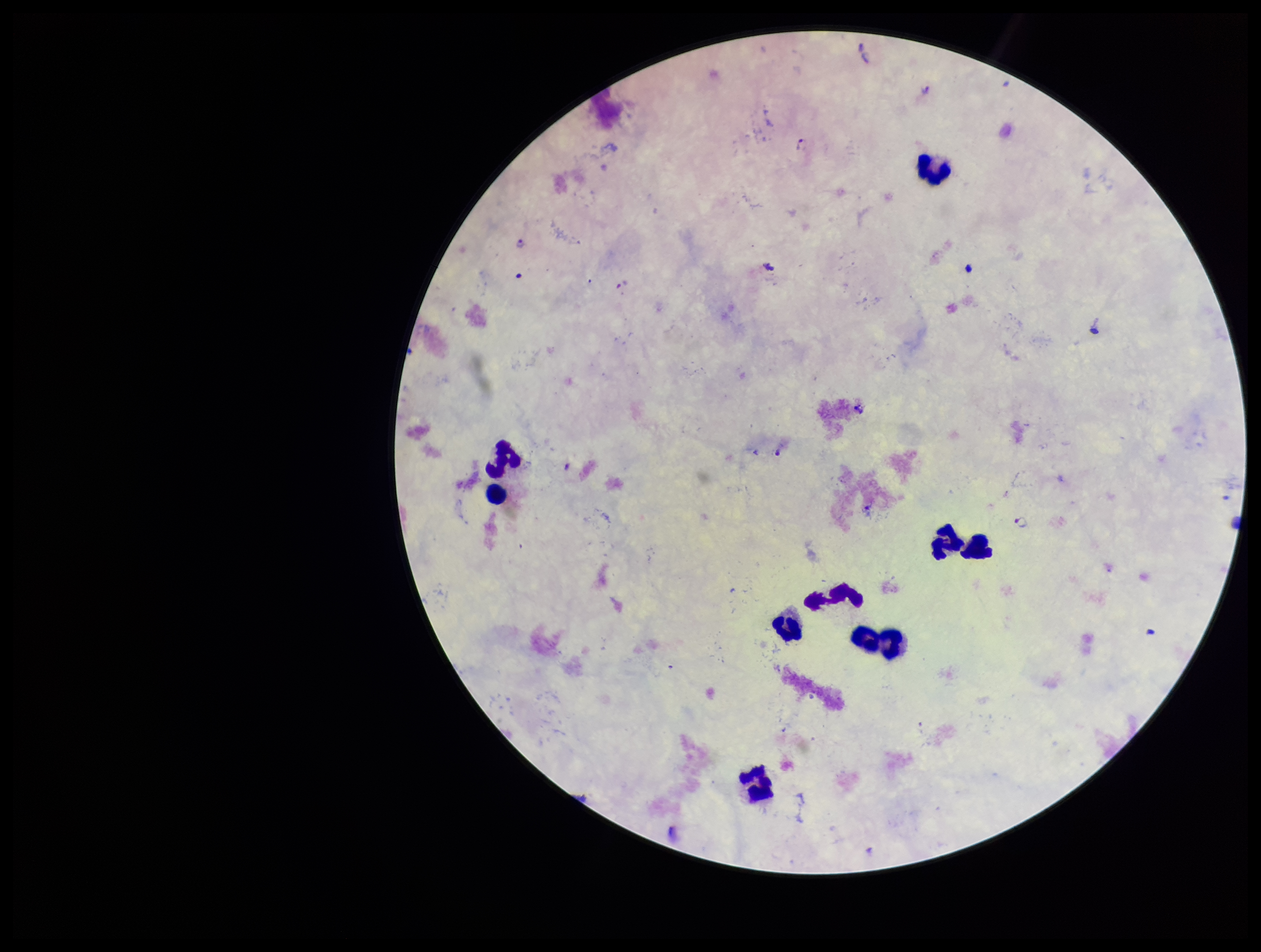

Stained with Giemsa. Species reported for this patient: Plasmodium falciparum. Photographed through the microscope eyepiece with a smartphone camera. Leukocyte count: 9. Parasite count: 6. Plasmodium parasites: seen. Image is 1261×952 pixels. Patient malaria status: infected. One field from this slide. Preparation: thick smear.